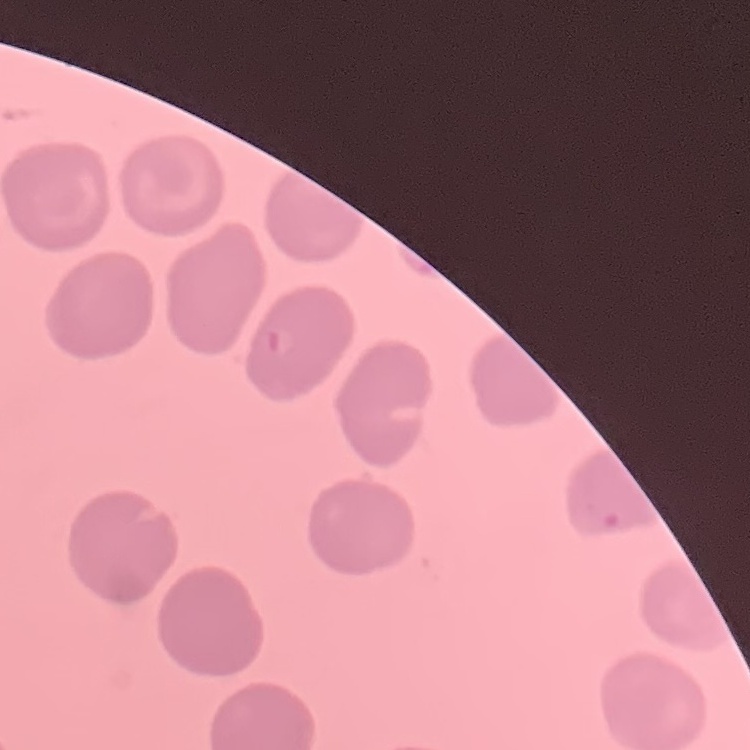

Summary:
  - Red blood cell morphology: no rouleaux formation
  - Stain: Field's or Giemsa
  - Image type: square crop of a larger photomicrograph
  - Preparation: thin blood smear